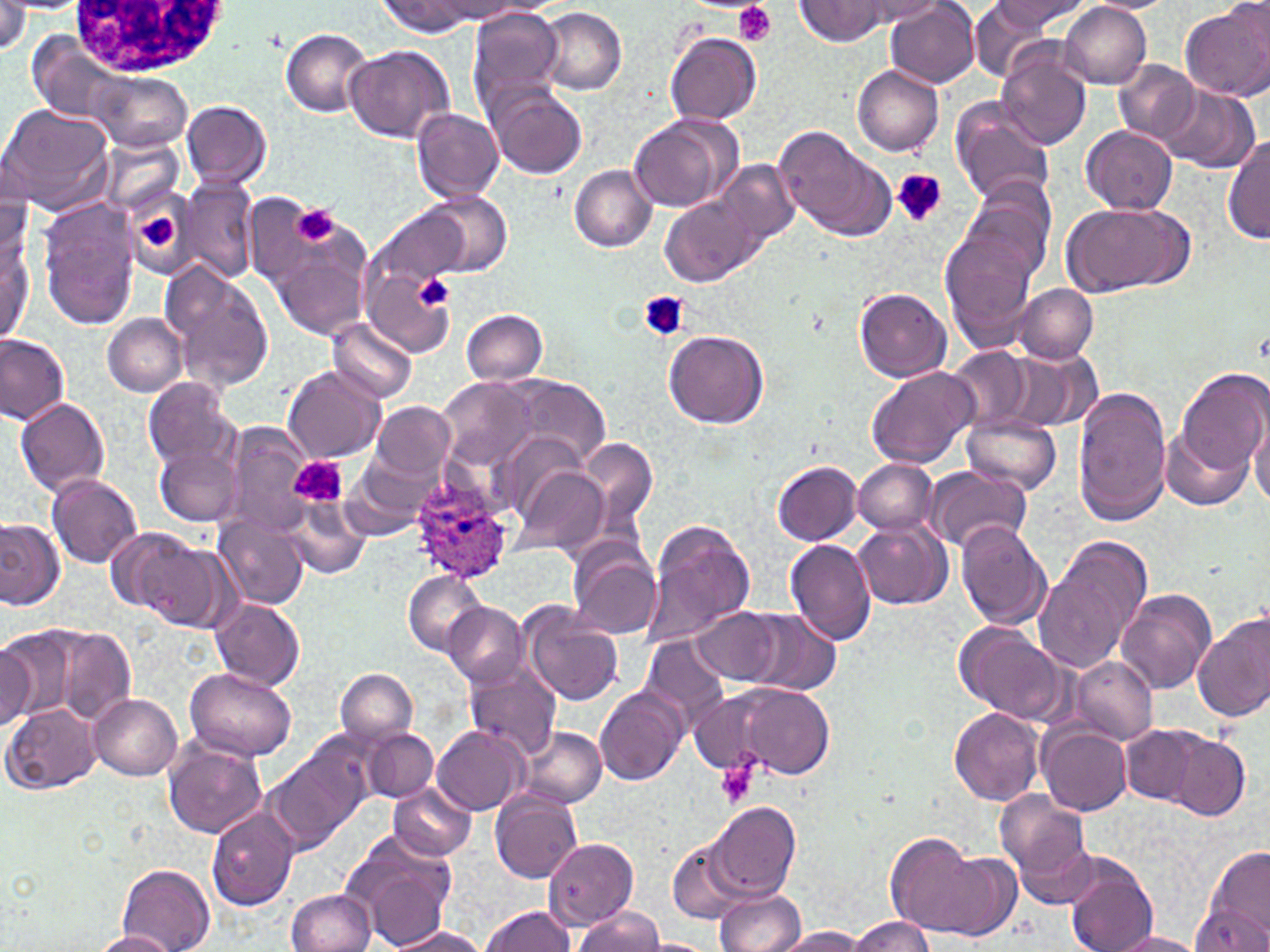 Approximate bounding boxes as [x1, y1, x2, y2] in pixels. Platelet locations: [734, 1, 775, 46], [891, 169, 946, 227], [291, 204, 339, 249], [137, 210, 180, 250], [413, 274, 453, 311], [639, 290, 689, 341], [288, 456, 347, 507], [714, 759, 760, 810]. White blood cell locations: [65, 0, 238, 76]. Uninfected red blood cell locations: [846, 0, 949, 28], [886, 0, 980, 87], [988, 0, 1093, 31], [1082, 0, 1172, 14], [0, 1, 29, 55], [377, 1, 482, 36], [424, 1, 524, 21], [795, 1, 892, 44], [1059, 1, 1151, 88], [966, 2, 1068, 78], [1178, 3, 1270, 103], [467, 6, 566, 115], [539, 8, 627, 94], [280, 28, 373, 116], [666, 31, 761, 125], [343, 45, 454, 143], [998, 47, 1092, 148], [1112, 61, 1200, 146], [852, 66, 945, 156], [83, 67, 194, 153], [1099, 67, 1236, 195], [487, 83, 589, 179], [1155, 83, 1259, 172], [180, 100, 273, 190], [949, 100, 1056, 207], [0, 103, 115, 214], [411, 108, 504, 201], [628, 114, 740, 214], [775, 122, 895, 241], [1081, 126, 1178, 215], [1223, 132, 1270, 246], [97, 135, 184, 216], [712, 156, 799, 252], [569, 165, 657, 251], [177, 179, 261, 285], [962, 182, 1057, 282], [424, 190, 512, 277], [660, 194, 762, 286], [38, 201, 140, 329], [1060, 202, 1191, 293], [378, 206, 468, 291], [939, 217, 1042, 352], [267, 221, 373, 341], [2, 230, 33, 346], [364, 257, 457, 356], [160, 262, 276, 393], [1015, 284, 1098, 363], [854, 287, 952, 382], [461, 309, 547, 385], [103, 314, 187, 395], [328, 317, 417, 405], [663, 329, 771, 428], [0, 333, 71, 425], [4, 339, 83, 489], [946, 346, 1039, 434], [1012, 349, 1102, 433], [283, 365, 385, 463], [866, 366, 980, 469], [1175, 367, 1268, 479], [142, 376, 240, 471], [440, 377, 535, 470], [513, 377, 610, 470], [1073, 388, 1172, 526], [14, 397, 112, 496], [370, 400, 456, 482], [963, 411, 1062, 494], [1250, 414, 1270, 509], [223, 422, 316, 534], [1160, 428, 1253, 512], [578, 436, 661, 540], [501, 437, 590, 528], [155, 444, 243, 526], [344, 448, 448, 539], [852, 458, 941, 535], [772, 460, 863, 545], [512, 463, 609, 557], [926, 466, 1033, 553], [46, 474, 143, 567], [281, 499, 370, 579], [214, 513, 310, 611], [0, 517, 64, 609], [641, 519, 755, 648], [852, 521, 951, 610], [955, 521, 1052, 631], [123, 533, 232, 629], [1033, 533, 1154, 677], [568, 539, 661, 639], [786, 539, 878, 645], [401, 571, 491, 656], [1116, 589, 1215, 694], [212, 599, 306, 689], [441, 601, 528, 687], [521, 607, 624, 706], [695, 607, 783, 686], [733, 609, 843, 697], [1193, 612, 1270, 722], [951, 622, 1075, 728], [0, 625, 76, 729], [51, 626, 136, 726], [641, 635, 731, 733], [0, 637, 38, 730], [1070, 656, 1158, 746], [464, 665, 561, 764], [186, 666, 297, 761], [335, 668, 418, 746], [721, 682, 835, 780], [595, 685, 688, 785], [88, 693, 184, 781], [3, 704, 100, 795], [948, 708, 1045, 805], [1038, 722, 1132, 816], [433, 726, 528, 814], [519, 726, 607, 810], [1118, 726, 1204, 805], [365, 729, 437, 802], [1156, 729, 1250, 819], [265, 738, 374, 852], [165, 741, 267, 837], [388, 781, 477, 862], [491, 788, 582, 884], [995, 790, 1092, 896], [709, 801, 800, 901], [204, 803, 300, 910], [340, 829, 456, 947], [885, 831, 993, 936], [544, 837, 638, 928], [668, 838, 752, 923], [1199, 846, 1270, 947], [1064, 860, 1158, 952], [118, 864, 216, 952], [285, 889, 376, 952], [715, 890, 805, 951], [476, 907, 579, 952], [573, 907, 667, 951], [849, 915, 938, 952], [383, 926, 493, 951], [771, 926, 869, 951], [92, 930, 180, 951], [1103, 931, 1209, 951]. Plasmodium ovale-infected red blood cell locations: [407, 476, 516, 584]. Slide-level diagnosis: Plasmodium ovale. Single field of view. Optical microscopy. Thin blood film. May-Grünwald-Giemsa-stained preparation. Image is 1270×952 pixels. Captured at 1000x magnification.